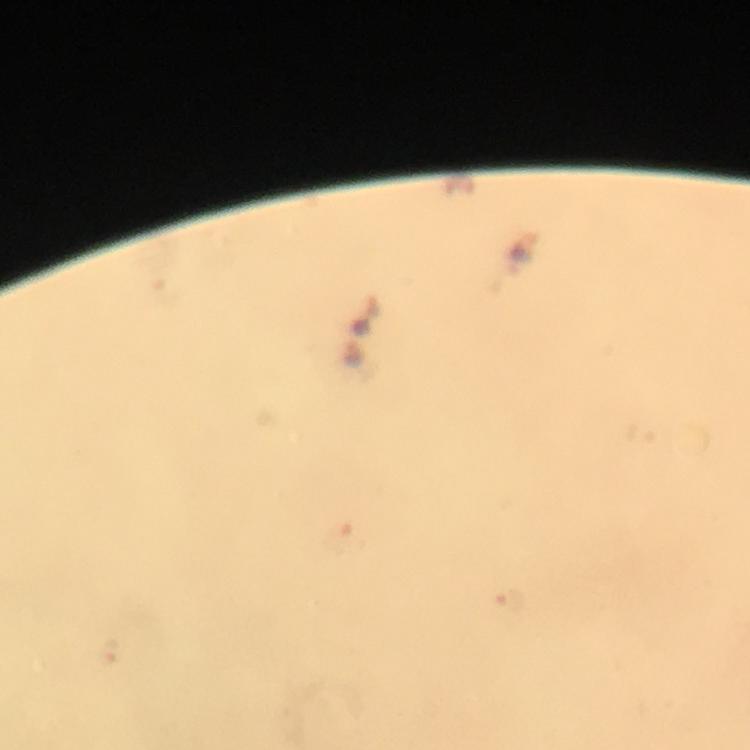
Approximate object centers, in pixels from the top-left corner.
Summary:
  - Plasmodium parasite locations: (x=344, y=535), (x=508, y=603), (x=108, y=650)
  - Stain: Giemsa
  - Context: from a diagnostic examination for malaria
  - Preparation: thick blood film
  - Magnification: 100x
  - Capture: smartphone mounted on the microscope
  - Cropped from: one field of view
  - Image size: 750×750 pixels
  - Immersion oil: used